Describe the morphology of the red blood cells.
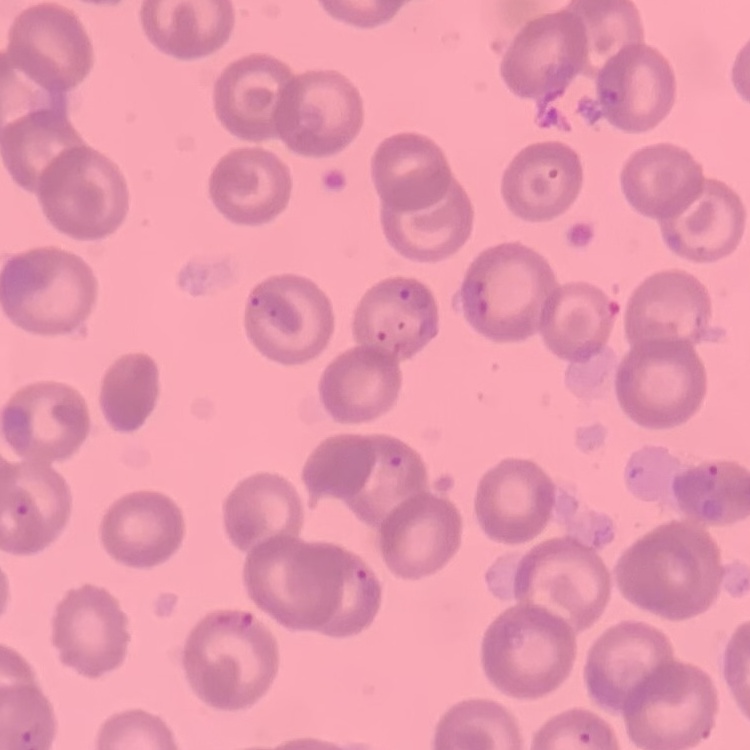
They show no rouleaux formation.

Thin blood film. One tile cut from a larger photomicrograph. Stained with either Field's or Giemsa.